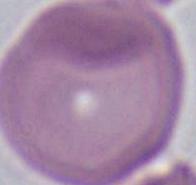

modality = micrograph
identification = erythrocyte
magnification = 1000x